Give the position of every leukocyte.
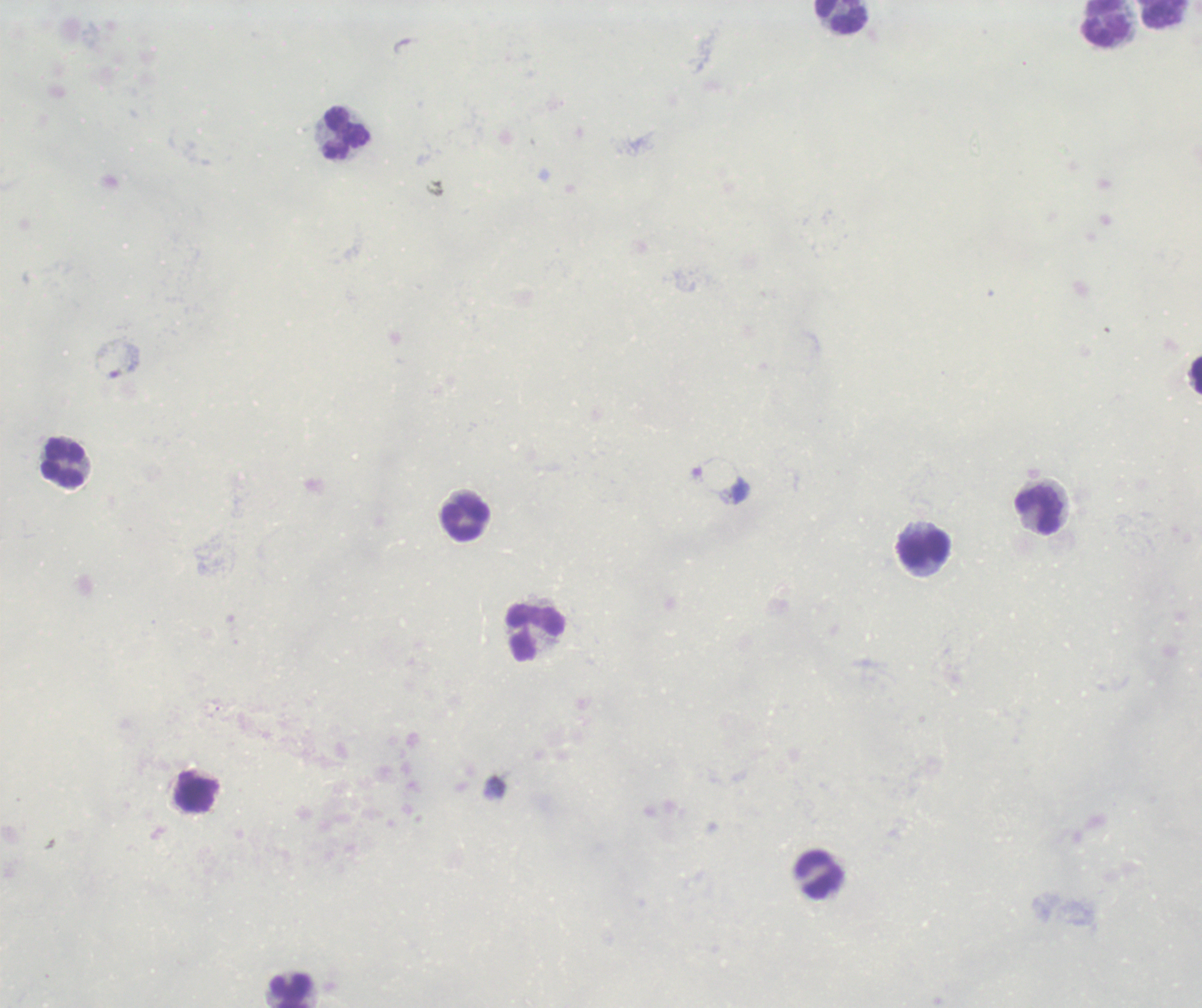

Approximate centers as (x, y) in pixels.
Leukocytes: (1165, 14), (841, 17), (1106, 23), (347, 133), (63, 463), (1039, 511), (466, 519), (925, 551), (535, 633), (196, 791), (819, 874), (290, 991).

Previously used in a real diagnosis. Romanowsky-stained preparation. Image is 1202×1008 pixels. Thick blood film. One field from this slide. Background quality: unsatisfactory. Captured at 100x magnification. Result: no malaria parasites seen.